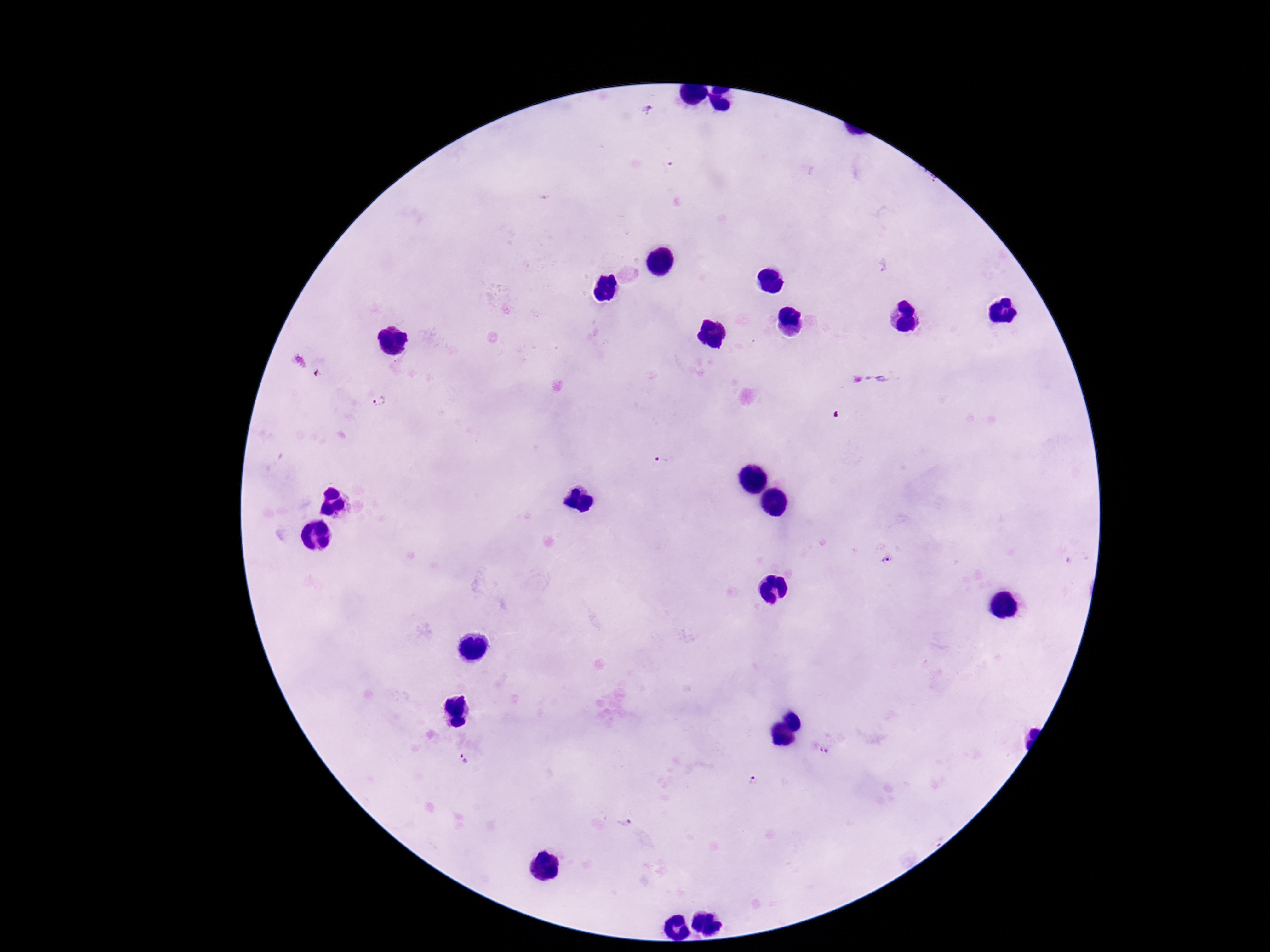 Approximate object centers, in pixels from the top-left corner. Plasmodium parasite locations: (x=649, y=110), (x=884, y=266), (x=882, y=379), (x=377, y=403), (x=661, y=460), (x=883, y=560), (x=826, y=751), (x=466, y=758), (x=754, y=779), (x=622, y=823). Giemsa stain. One field from this slide. 100x magnification. Patient malaria status: positive. Smartphone photograph taken through the microscope eyepiece. Thick blood smear. Image is 1270×952 pixels.